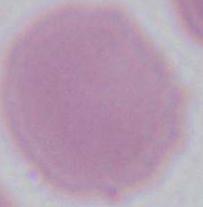

{
  "identification": "erythrocyte",
  "magnification": "1000x",
  "modality": "micrograph"
}